Identify the parasite.
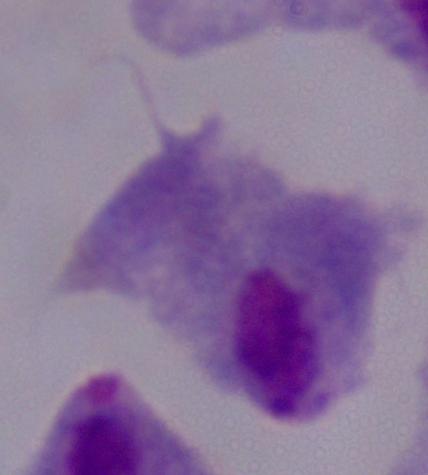
This is a trichomonad.

{
  "magnification": "1000x",
  "modality": "photomicrograph"
}